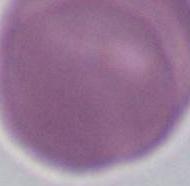 Photomicrograph. A red blood cell is shown. 1000x magnification.